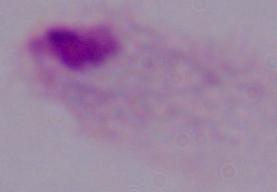 Captured at 1000x magnification. A trichomonad is seen. Photomicrograph.